Describe the morphology of the red blood cells.
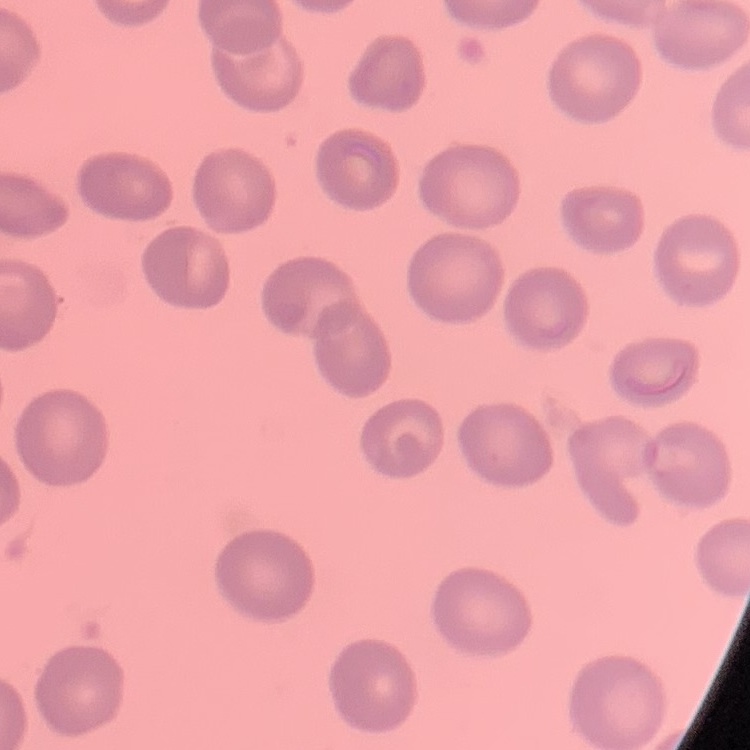
They show no rouleaux formation.

Thin blood smear. Field's or Giemsa stain. Square crop of a larger photomicrograph.